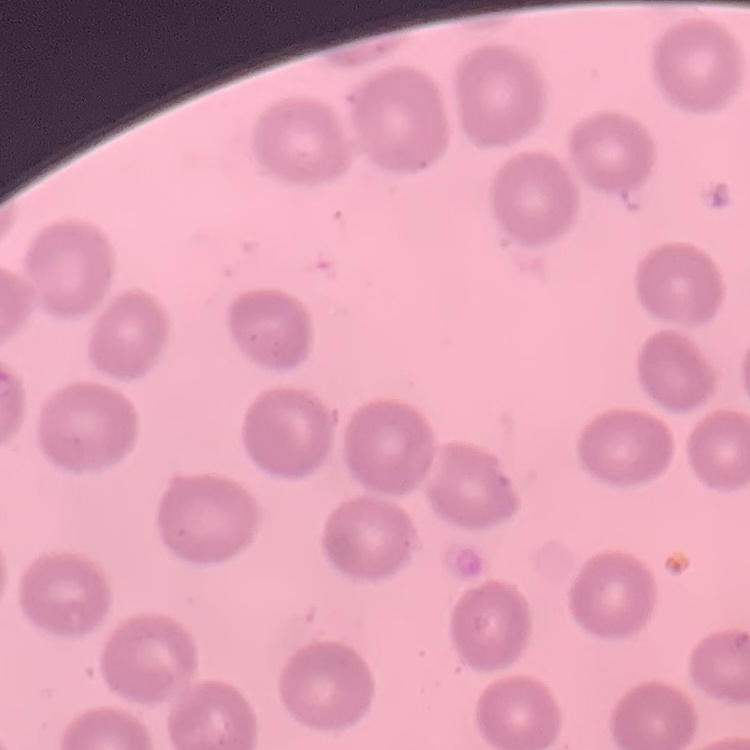
erythrocyte morphology = no rouleaux formation
image type = one tile cut from a larger photomicrograph
stain = Field's or Giemsa
preparation = thin peripheral smear